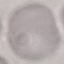

Result: no malaria parasites seen. Automatically extracted cell patch, resized to 64 × 64 pixels. Thin smear of blood. Giemsa stain. Acquired by smartphone through the microscope eyepiece.